Identify the parasite.
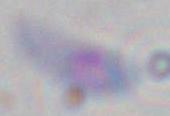
This is Toxoplasma gondii.

Summary:
  - Magnification: 1000x
  - Modality: photomicrograph